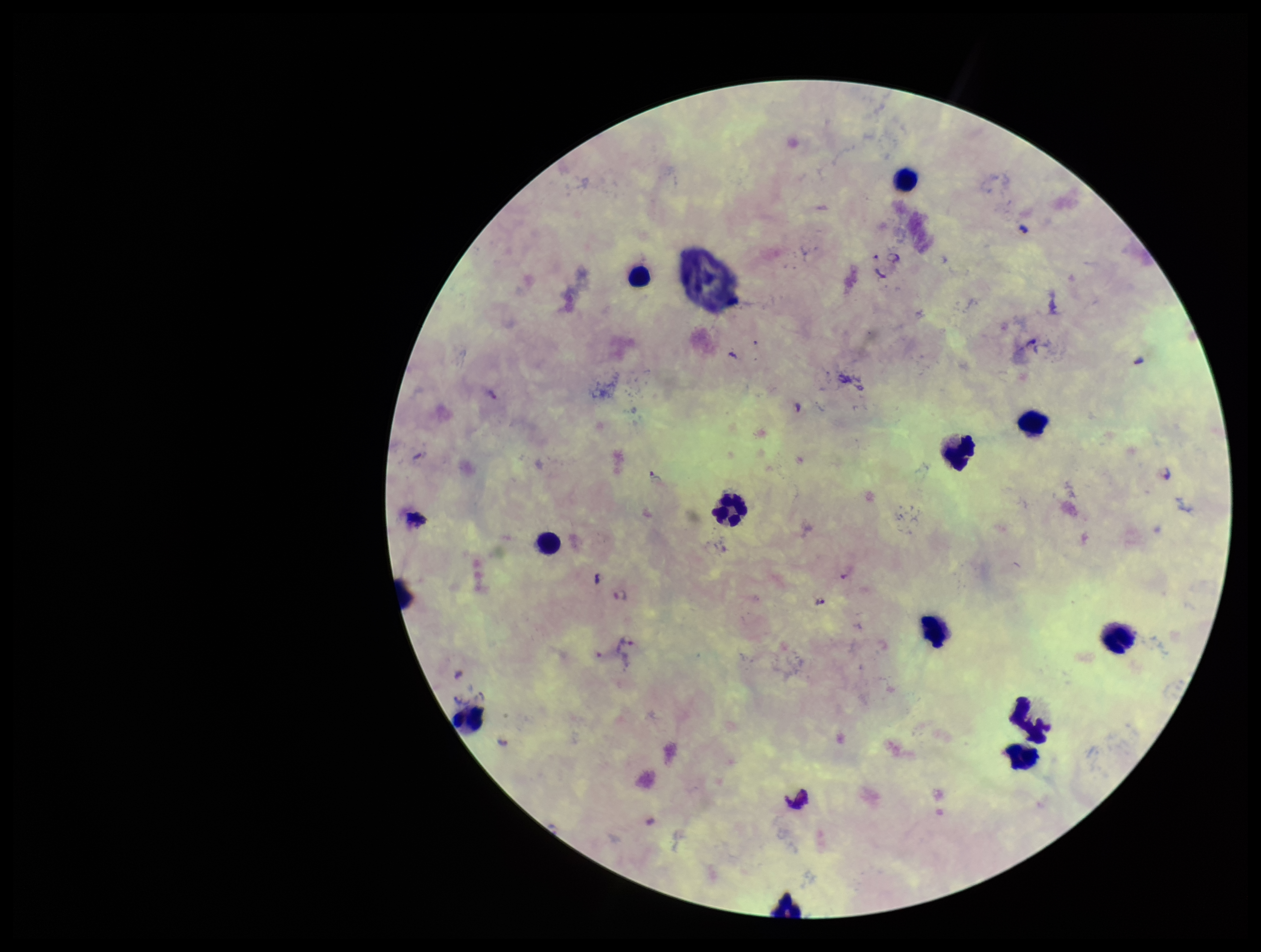 One field from this slide. Giemsa stain. Photographed through the microscope eyepiece with a smartphone camera. Image is 1261×952 pixels. Patient malaria status: infected. Preparation: thick blood smear. Plasmodium parasites: seen. Leukocyte count: 12. Parasite count: 3. Species reported for this patient: Plasmodium falciparum.